State which parasite is depicted.
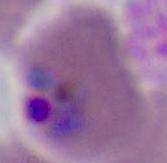

Plasmodium.

magnification = 400x or 1000x
modality = photomicrograph